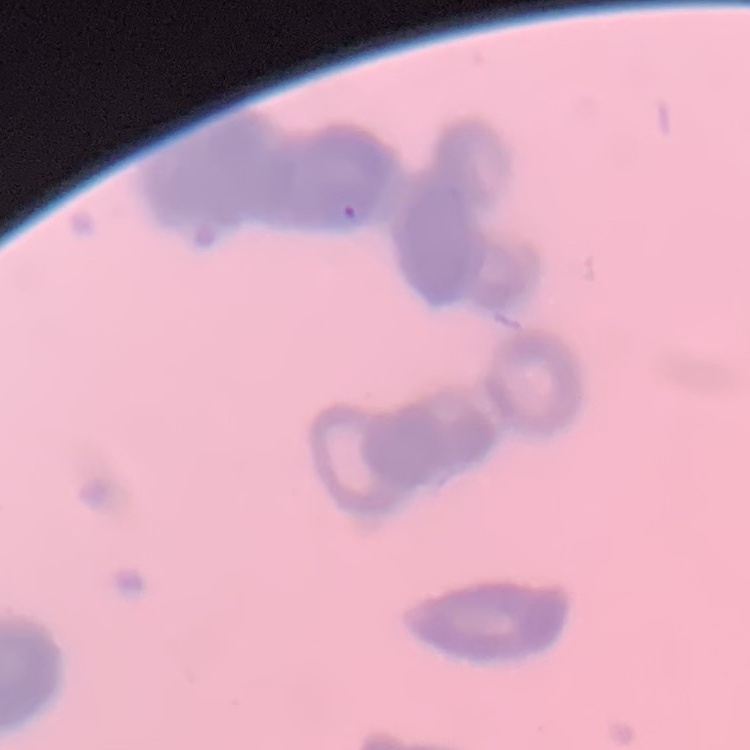

Summary:
  - Red blood cell morphology: rouleaux formation
  - Preparation: thin blood film
  - Image type: one tile cut from a larger photomicrograph
  - Stain: Field's or Giemsa